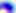

magnification = 400x
identification = Toxoplasma gondii
modality = micrograph